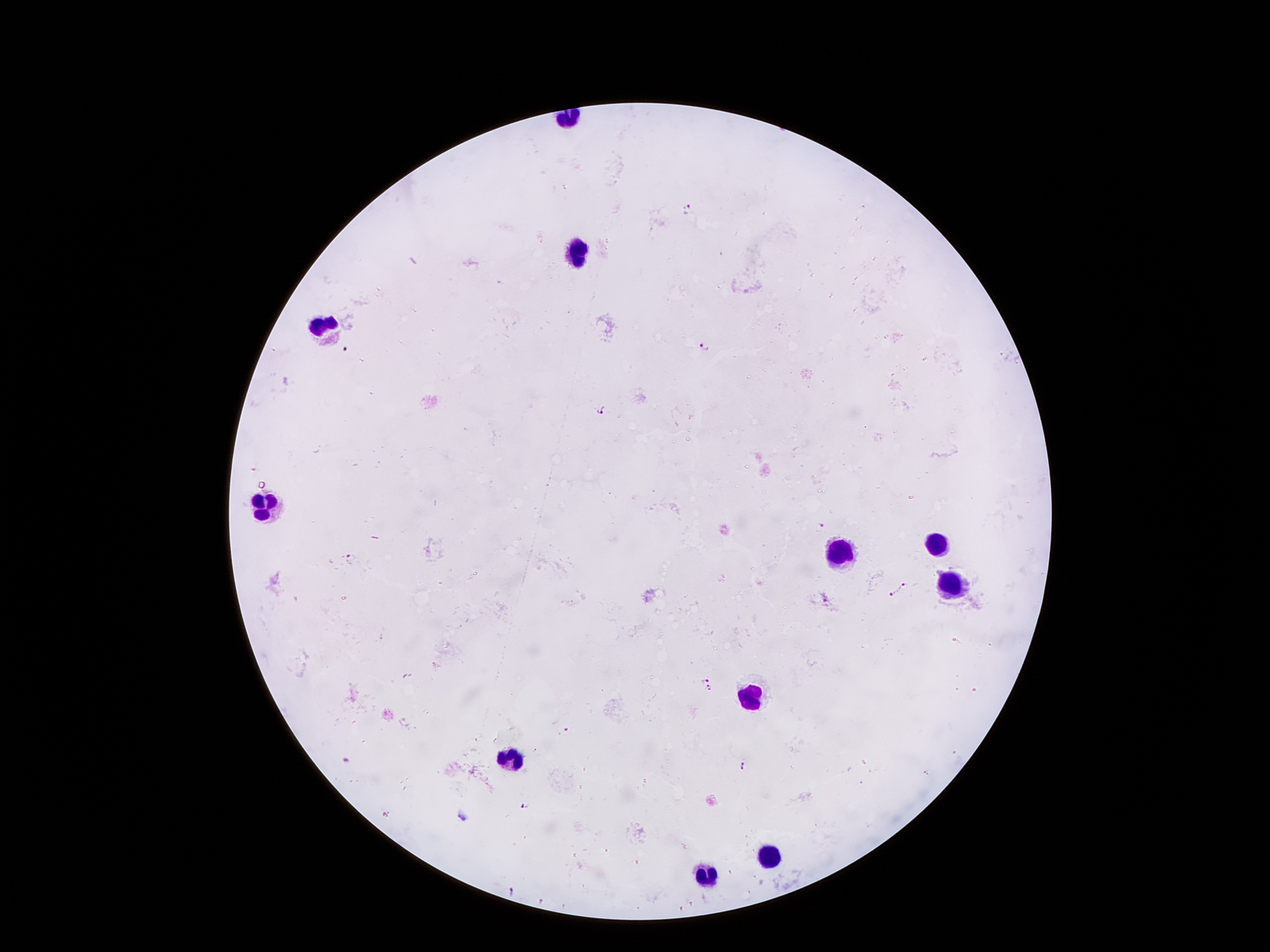

patient_malaria_status: infected with Plasmodium falciparum
image_size: 1270×952 pixels
magnification: 100x
stain: Giemsa
field_of_view: single
plasmodium_parasite_locations: 'approximate centers as {x, y} in pixels: {688, 210}, {704, 345}, {603, 409}, {823, 528}, {350, 558}, {902, 585}, {888, 595}, {706, 679}, {709, 689}, {565, 730}, {347, 761}, {742, 765}, {525, 805}, {461, 815}, {511, 890}'
preparation: thick blood film
leukocyte_locations: 'approximate centers as {x, y} in pixels: {578, 249}, {322, 331}, {267, 505}, {939, 539}, {837, 550}, {946, 584}, {748, 696}, {511, 759}, {765, 854}, {704, 876}'
capture: smartphone through the microscope eyepiece